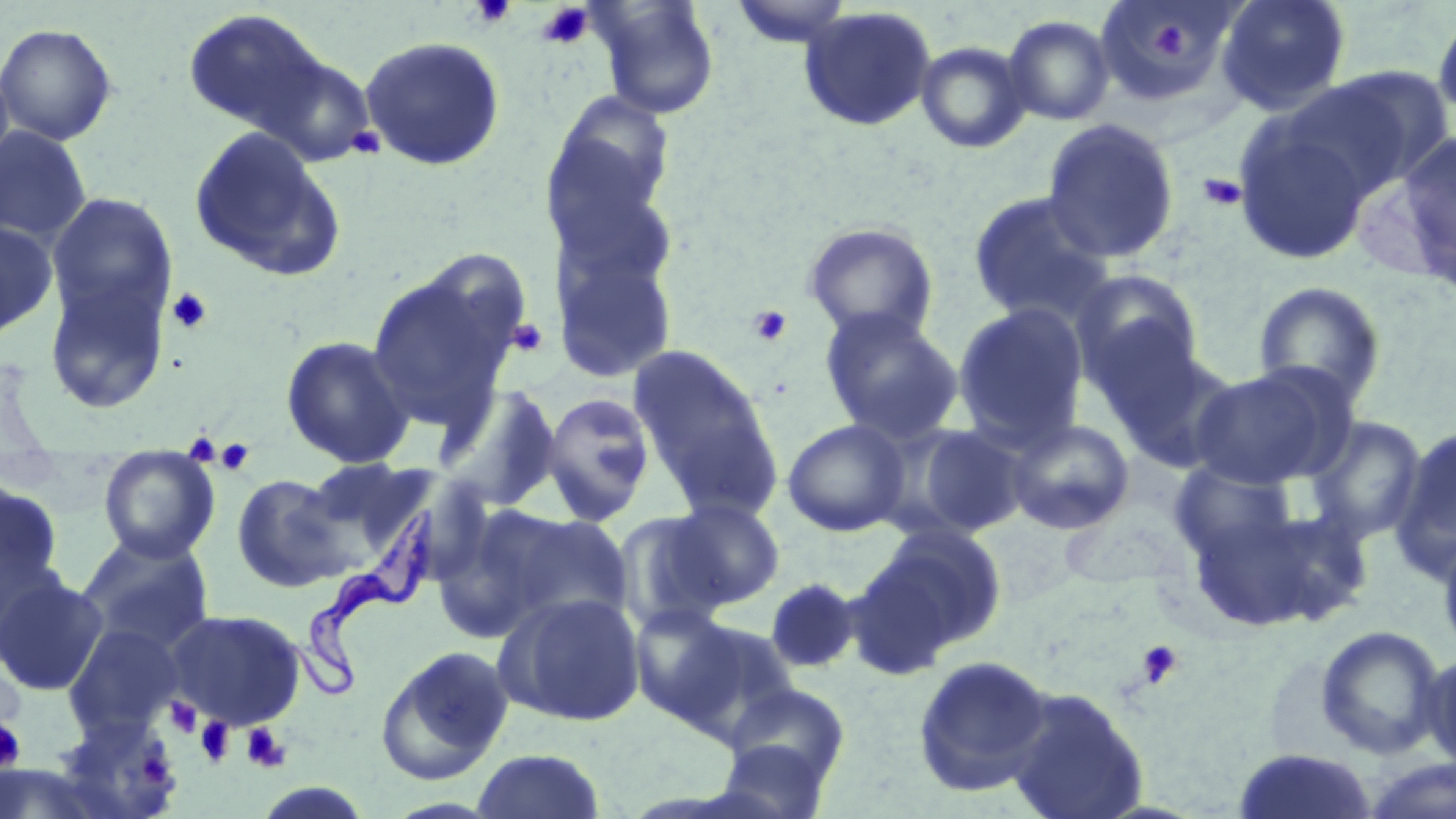

Approximate bounding boxes as named x1/y1/x2/y2 corners in pixels. Uninfected red blood cell locations: (x1=592, y1=0, x2=720, y2=119), (x1=728, y1=0, x2=856, y2=49), (x1=1215, y1=0, x2=1351, y2=114), (x1=1094, y1=1, x2=1240, y2=108), (x1=799, y1=6, x2=938, y2=132), (x1=182, y1=8, x2=330, y2=136), (x1=1431, y1=8, x2=1456, y2=127), (x1=1002, y1=14, x2=1115, y2=126), (x1=0, y1=22, x2=118, y2=146), (x1=359, y1=36, x2=505, y2=171), (x1=915, y1=40, x2=1032, y2=153), (x1=254, y1=51, x2=378, y2=167), (x1=0, y1=58, x2=16, y2=185), (x1=1298, y1=66, x2=1451, y2=198), (x1=545, y1=93, x2=675, y2=232), (x1=1232, y1=111, x2=1379, y2=265), (x1=1041, y1=117, x2=1180, y2=263), (x1=0, y1=126, x2=92, y2=244), (x1=187, y1=126, x2=343, y2=280), (x1=1393, y1=129, x2=1456, y2=290), (x1=550, y1=168, x2=681, y2=296), (x1=967, y1=191, x2=1115, y2=327), (x1=46, y1=192, x2=178, y2=326), (x1=0, y1=219, x2=58, y2=340), (x1=802, y1=222, x2=939, y2=343), (x1=552, y1=253, x2=678, y2=384), (x1=365, y1=263, x2=522, y2=430), (x1=43, y1=266, x2=173, y2=414), (x1=1070, y1=268, x2=1204, y2=399), (x1=1252, y1=281, x2=1387, y2=408), (x1=951, y1=302, x2=1090, y2=449), (x1=819, y1=307, x2=965, y2=445), (x1=280, y1=335, x2=415, y2=469), (x1=1103, y1=338, x2=1243, y2=472), (x1=627, y1=344, x2=780, y2=506), (x1=1188, y1=363, x2=1353, y2=490), (x1=436, y1=383, x2=562, y2=511), (x1=539, y1=391, x2=657, y2=526), (x1=1303, y1=415, x2=1428, y2=546), (x1=1004, y1=417, x2=1135, y2=535), (x1=782, y1=418, x2=911, y2=537), (x1=899, y1=422, x2=1031, y2=538), (x1=1390, y1=426, x2=1456, y2=580), (x1=97, y1=452, x2=221, y2=563), (x1=300, y1=456, x2=432, y2=562), (x1=1167, y1=459, x2=1300, y2=567), (x1=231, y1=473, x2=352, y2=593), (x1=0, y1=475, x2=66, y2=620), (x1=1181, y1=496, x2=1366, y2=635), (x1=665, y1=498, x2=785, y2=608), (x1=485, y1=508, x2=635, y2=631), (x1=612, y1=510, x2=734, y2=634), (x1=864, y1=523, x2=1007, y2=658), (x1=1437, y1=531, x2=1456, y2=662), (x1=76, y1=532, x2=215, y2=655), (x1=0, y1=572, x2=109, y2=697), (x1=764, y1=577, x2=862, y2=675), (x1=495, y1=591, x2=646, y2=727), (x1=630, y1=603, x2=741, y2=724), (x1=167, y1=609, x2=307, y2=731), (x1=673, y1=619, x2=800, y2=741), (x1=62, y1=623, x2=185, y2=738), (x1=1314, y1=624, x2=1446, y2=760), (x1=375, y1=645, x2=515, y2=784), (x1=1420, y1=650, x2=1456, y2=776), (x1=912, y1=654, x2=1054, y2=798), (x1=724, y1=683, x2=851, y2=789), (x1=1004, y1=685, x2=1149, y2=819), (x1=48, y1=712, x2=183, y2=819), (x1=714, y1=738, x2=831, y2=819), (x1=470, y1=748, x2=607, y2=818), (x1=1233, y1=749, x2=1378, y2=819), (x1=1360, y1=757, x2=1456, y2=819). Platelet locations: (x1=469, y1=0, x2=516, y2=28), (x1=538, y1=3, x2=593, y2=49), (x1=1151, y1=20, x2=1188, y2=62), (x1=345, y1=126, x2=387, y2=160), (x1=1197, y1=173, x2=1247, y2=212), (x1=166, y1=286, x2=214, y2=334), (x1=747, y1=304, x2=793, y2=347), (x1=506, y1=318, x2=549, y2=358), (x1=214, y1=440, x2=256, y2=476), (x1=1136, y1=640, x2=1184, y2=689), (x1=165, y1=698, x2=203, y2=738), (x1=0, y1=716, x2=26, y2=774), (x1=196, y1=717, x2=236, y2=766), (x1=241, y1=723, x2=290, y2=773), (x1=136, y1=754, x2=172, y2=786). Trypanosoma brucei locations: (x1=286, y1=507, x2=436, y2=706). Slide-level diagnosis: Trypanosoma brucei. Optical microscopy. May-Grünwald-Giemsa-stained preparation. 1000x magnification. Image is 1456×819 pixels. Single field of view. Thin blood film.